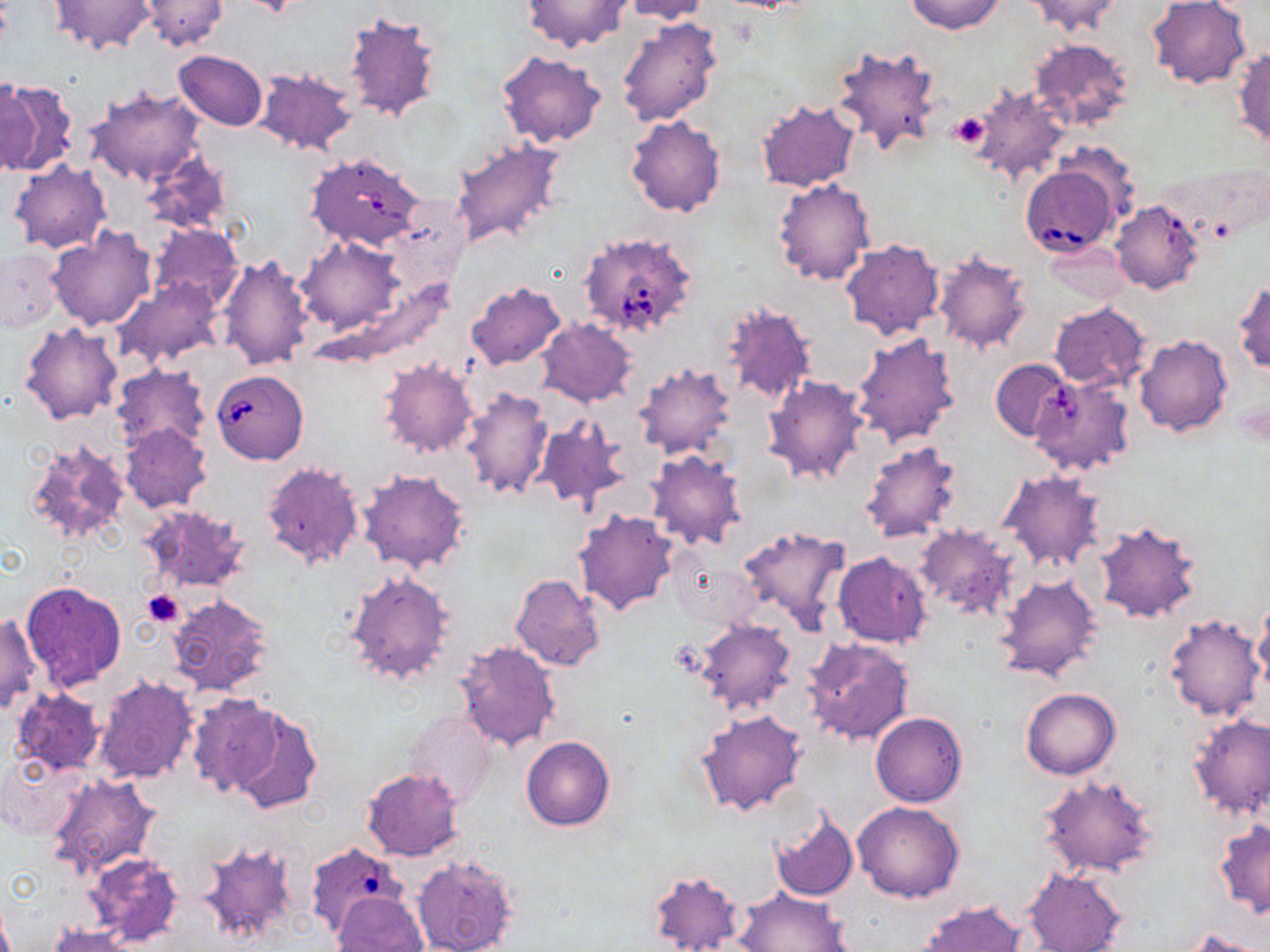 Approximate bounding boxes as (x1,y1)-(x2,y2) corner pairs in pixels. Babesia divergens-infected red blood cell locations: (306,152)-(425,250), (1021,164)-(1121,256), (576,231)-(697,338), (210,369)-(308,464), (307,844)-(408,940). Platelet locations: (948,111)-(990,149), (142,589)-(186,626), (671,638)-(706,675). Uninfected red blood cell locations: (137,0)-(227,50), (618,0)-(711,23), (905,0)-(1005,35), (1024,0)-(1125,36), (1148,0)-(1251,89), (47,1)-(158,57), (520,1)-(633,53), (341,13)-(442,125), (616,15)-(723,128), (1030,39)-(1136,133), (829,45)-(942,158), (1232,46)-(1270,151), (497,50)-(605,149), (172,51)-(267,130), (253,68)-(359,156), (0,81)-(78,175), (969,84)-(1070,187), (85,87)-(208,187), (756,98)-(863,193), (625,115)-(727,218), (450,141)-(565,255), (141,151)-(232,234), (9,159)-(110,254), (772,178)-(874,288), (1110,200)-(1202,294), (149,223)-(241,311), (47,226)-(156,331), (296,239)-(402,335), (841,239)-(947,341), (1043,242)-(1131,306), (1,247)-(64,331), (932,249)-(1032,354), (216,254)-(315,370), (116,278)-(221,370), (326,279)-(455,367), (466,280)-(567,372), (1233,280)-(1269,375), (721,301)-(817,407), (1048,303)-(1151,390), (537,318)-(637,408), (19,321)-(125,426), (850,331)-(960,448), (1135,335)-(1234,437), (764,351)-(948,469), (379,358)-(479,458), (991,359)-(1072,441), (632,363)-(737,461), (112,365)-(211,452), (763,376)-(869,485), (459,387)-(553,502), (534,415)-(631,511), (121,423)-(212,513), (22,437)-(131,547), (858,440)-(964,544), (645,448)-(747,551), (261,461)-(364,572), (359,469)-(469,573), (998,470)-(1105,572), (141,505)-(250,594), (574,508)-(680,617), (1093,522)-(1204,625), (913,524)-(1022,619), (734,525)-(850,634), (832,551)-(932,648), (344,570)-(454,685), (995,573)-(1102,684), (510,574)-(605,671), (20,581)-(126,691), (165,593)-(275,699), (1254,598)-(1270,690), (0,612)-(41,715), (1164,614)-(1266,722), (692,618)-(797,716), (801,635)-(916,747), (454,640)-(561,753), (93,675)-(198,784), (13,688)-(105,775), (1023,688)-(1120,779), (184,693)-(285,796), (224,706)-(323,813), (696,709)-(807,817), (870,712)-(966,806), (1188,714)-(1270,823), (522,736)-(614,831), (2,755)-(82,839), (362,768)-(464,861), (45,772)-(160,879), (1037,772)-(1160,879), (853,801)-(965,902), (769,810)-(859,901), (1215,820)-(1270,919), (196,839)-(301,951), (83,851)-(186,949), (411,854)-(521,952), (1022,867)-(1127,952), (646,869)-(744,952), (734,887)-(850,951), (332,893)-(427,952), (918,900)-(1029,952), (45,924)-(136,952), (1178,930)-(1267,952). Slide-level diagnosis: Babesia divergens. 1000x magnification. Image is 1270×952 pixels. Single field of view. Thin blood film. Light microscopy. May-Grünwald-Giemsa stain.